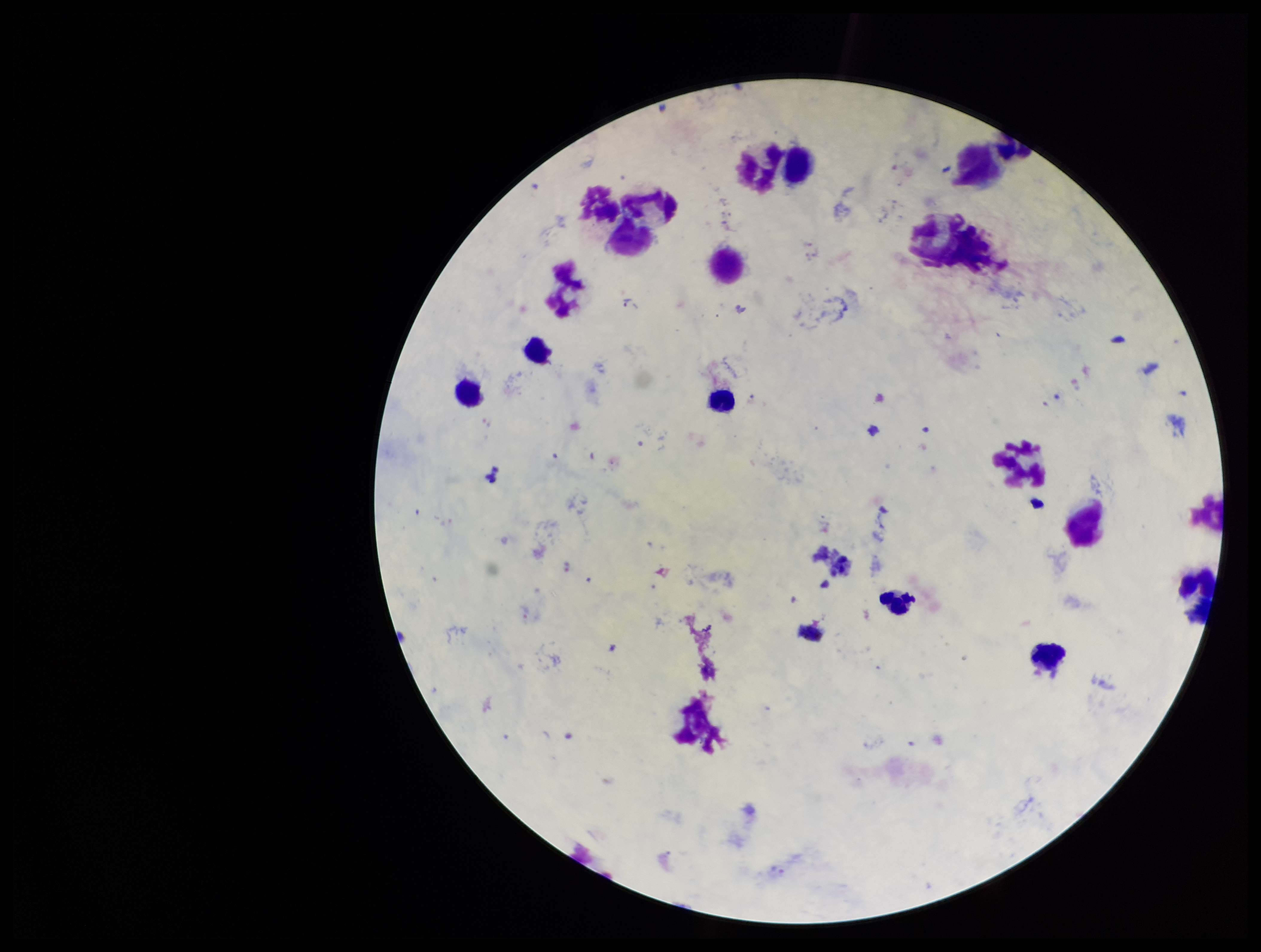

Species reported for this patient: Plasmodium vivax. Image is 1261×952 pixels. Stained with Giemsa. Leukocyte count: 16. Single field of view. Photographed through the microscope eyepiece with a smartphone camera. Plasmodium parasites: identified. Preparation: thick smear. Patient malaria status: positive. Parasite count: 1.